Outline each Plasmodium falciparum-infected red blood cell.
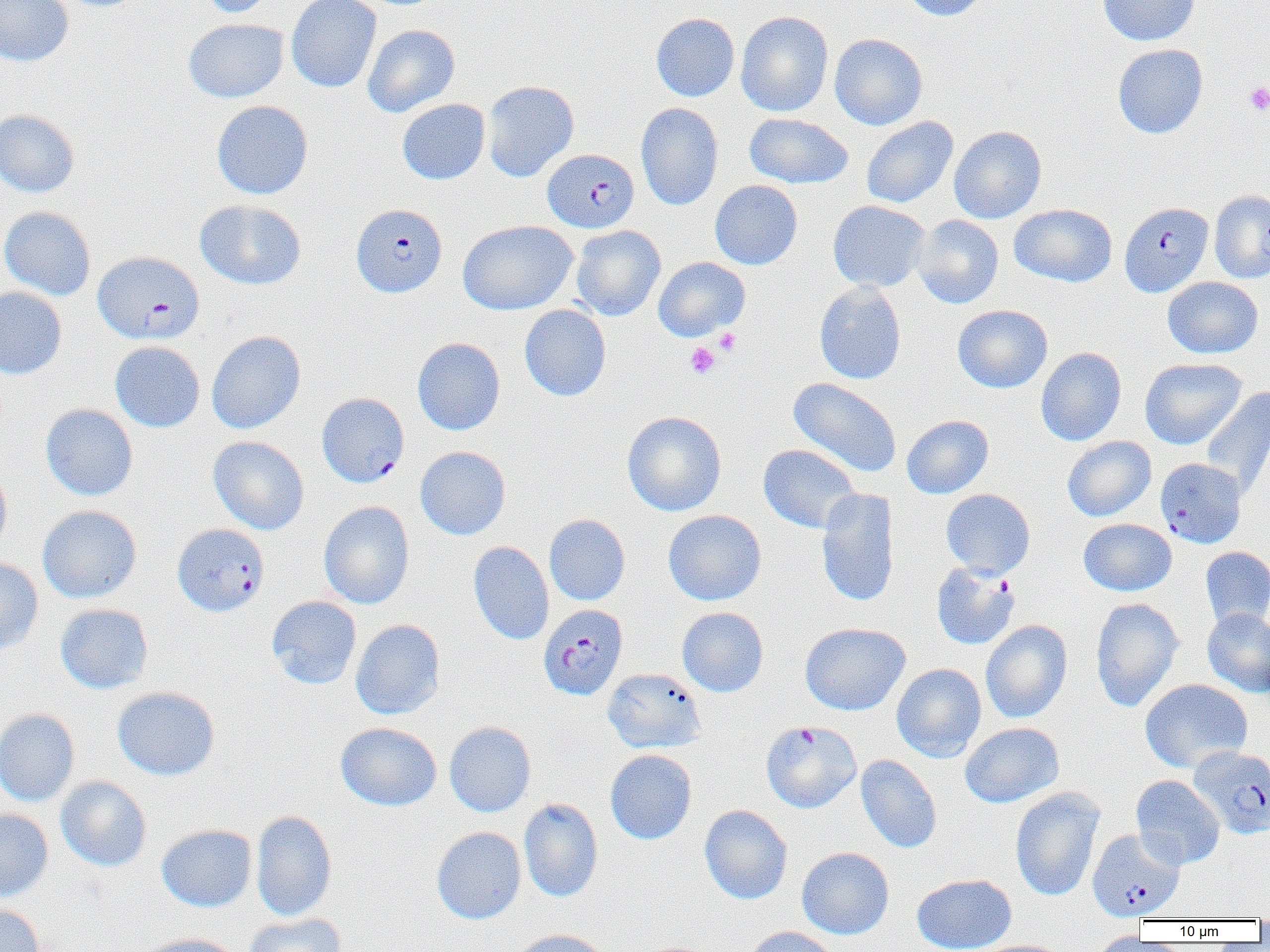

Approximate bounding boxes as [x1, y1, x2, y2] in pixels.
Plasmodium falciparum-infected red blood cells (subset): [543, 149, 639, 232], [1119, 201, 1213, 297], [351, 203, 447, 297], [92, 251, 204, 345], [317, 394, 409, 489], [172, 523, 269, 617], [931, 563, 1020, 650], [535, 605, 626, 702], [761, 720, 861, 813], [1189, 745, 1270, 839], [1088, 828, 1185, 920].

Summary:
  - Platelet locations: [1244, 82, 1270, 115], [714, 328, 741, 355], [685, 342, 720, 379]
  - Uninfected red blood cell locations (subset): [0, 0, 73, 66], [194, 0, 276, 18], [286, 0, 382, 93], [900, 0, 991, 21], [1097, 0, 1199, 46], [735, 10, 834, 117], [650, 12, 740, 102], [182, 18, 289, 103], [362, 24, 460, 117], [829, 33, 928, 130], [1112, 43, 1208, 139], [482, 80, 579, 182], [397, 99, 490, 185], [211, 100, 313, 199], [636, 103, 724, 211], [0, 109, 79, 197], [743, 113, 853, 189], [861, 116, 958, 208], [949, 125, 1046, 223], [710, 180, 802, 270], [1209, 190, 1270, 283], [195, 199, 307, 290], [828, 200, 930, 292], [1009, 204, 1118, 287], [0, 206, 96, 300], [913, 215, 1004, 309], [457, 220, 578, 314], [571, 225, 666, 321], [653, 257, 749, 341], [1162, 276, 1263, 358], [814, 282, 906, 384], [0, 286, 67, 378], [519, 304, 611, 402], [953, 304, 1053, 393], [206, 331, 305, 434], [412, 337, 505, 435], [110, 341, 205, 432], [1036, 347, 1126, 446], [1140, 357, 1246, 450], [787, 377, 901, 477], [1200, 386, 1270, 498], [40, 403, 138, 501], [622, 410, 727, 516], [902, 415, 993, 499], [208, 436, 309, 535], [1062, 436, 1156, 522], [758, 443, 860, 534], [414, 446, 511, 540], [0, 463, 12, 557], [816, 488, 900, 606], [941, 488, 1036, 579], [318, 501, 415, 609], [37, 505, 142, 603], [663, 510, 766, 605], [544, 514, 630, 605], [1078, 518, 1177, 596], [468, 541, 554, 645], [1201, 546, 1270, 631], [0, 557, 44, 657], [266, 595, 362, 689], [1090, 597, 1183, 712], [55, 603, 153, 694], [677, 607, 768, 697], [1202, 608, 1270, 697], [350, 619, 446, 720], [980, 619, 1072, 723], [799, 622, 911, 716], [891, 663, 986, 762], [602, 668, 707, 754], [1140, 678, 1252, 772], [112, 686, 220, 780], [0, 708, 80, 807], [335, 721, 442, 811], [444, 721, 536, 817], [959, 722, 1064, 808], [605, 749, 697, 844], [856, 754, 941, 853], [1130, 775, 1225, 869], [55, 776, 152, 872], [1010, 787, 1105, 902], [518, 798, 603, 902], [699, 804, 793, 904], [0, 809, 53, 902], [251, 810, 337, 921], [156, 824, 257, 911], [431, 826, 526, 924], [796, 847, 894, 939], [912, 873, 1017, 952], [0, 903, 45, 952], [242, 913, 346, 952], [745, 926, 839, 952], [510, 929, 612, 952], [1093, 931, 1172, 952], [136, 934, 244, 952], [975, 939, 1071, 952]
  - Slide-level diagnosis: Plasmodium falciparum
  - Image size: 1270×952 pixels
  - Field of view: one of a larger specimen
  - Modality: light microscopy
  - Magnification: 1000x
  - Preparation: thin blood film